Classify this cell by malaria status.
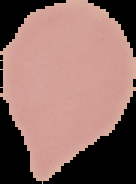

Uninfected.

image size = 136×184 pixels
image type = cell region segmented out of the field of view; surrounding area masked to black
preparation = thin blood film